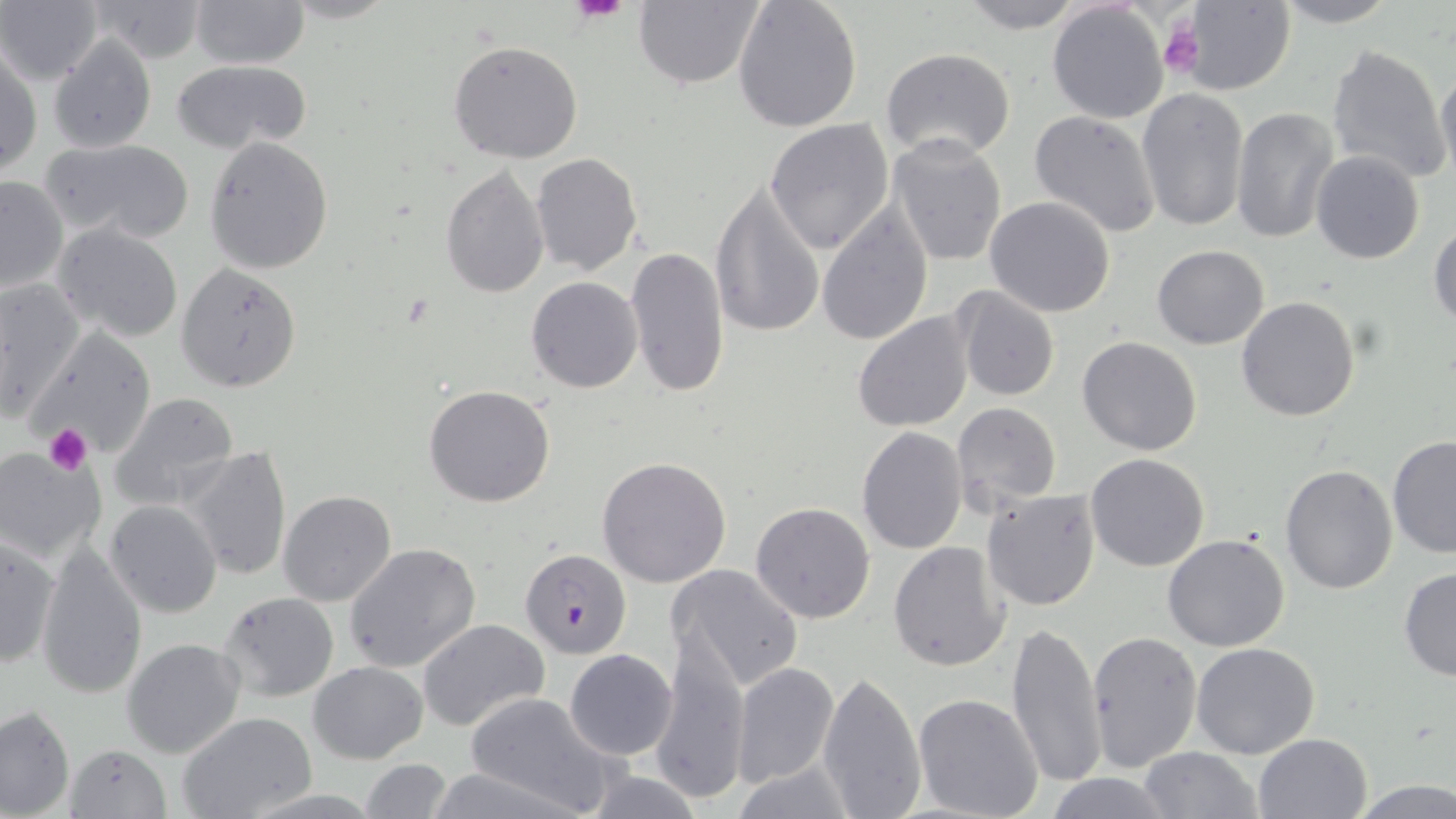
Summary:
  - Coordinate format: approximate bounding boxes as (x1, y1, x2, y2) in pixels
  - Uninfected red blood cell locations: (93, 0, 209, 64), (189, 0, 308, 69), (632, 0, 764, 89), (732, 0, 862, 134), (957, 0, 1086, 33), (1270, 0, 1403, 27), (2, 1, 102, 86), (1181, 1, 1294, 95), (1047, 3, 1170, 125), (48, 33, 156, 152), (448, 40, 583, 164), (1326, 43, 1450, 184), (2, 45, 42, 178), (880, 47, 1016, 161), (172, 58, 311, 154), (1435, 68, 1456, 185), (1136, 87, 1252, 234), (1230, 108, 1340, 245), (1030, 111, 1162, 237), (764, 119, 895, 255), (886, 134, 1008, 269), (42, 138, 194, 243), (205, 138, 332, 274), (1311, 150, 1425, 264), (531, 154, 642, 276), (440, 164, 549, 298), (0, 177, 67, 294), (710, 181, 827, 341), (984, 196, 1116, 318), (815, 202, 935, 348), (1428, 220, 1456, 329), (51, 223, 185, 346), (1152, 244, 1270, 348), (625, 246, 730, 398), (177, 261, 304, 394), (525, 275, 643, 394), (1, 277, 86, 420), (951, 286, 1059, 400), (1236, 297, 1361, 422), (851, 309, 976, 432), (32, 329, 159, 459), (1077, 336, 1204, 456), (424, 384, 555, 507), (109, 393, 240, 511), (953, 402, 1061, 511), (857, 425, 968, 555), (1388, 435, 1456, 560), (184, 445, 293, 582), (0, 448, 106, 567), (1085, 453, 1211, 572), (596, 456, 732, 588), (1281, 463, 1400, 595), (981, 488, 1103, 612), (277, 490, 397, 606), (106, 500, 223, 617), (751, 501, 875, 623), (0, 533, 59, 671), (1162, 533, 1291, 653), (36, 539, 147, 702), (887, 541, 1011, 671), (343, 542, 480, 672), (667, 563, 805, 694), (1398, 566, 1456, 682), (217, 591, 339, 703), (416, 618, 550, 732), (1008, 620, 1104, 791), (651, 630, 752, 806), (1088, 630, 1202, 771), (121, 637, 246, 757), (1190, 642, 1321, 759), (564, 649, 678, 760), (308, 660, 428, 766), (731, 663, 839, 788), (815, 668, 927, 819), (463, 691, 620, 818), (912, 693, 1043, 819), (0, 704, 75, 818), (176, 712, 317, 819), (1252, 731, 1373, 819), (65, 743, 173, 819), (1138, 747, 1263, 819), (357, 759, 453, 819), (728, 759, 856, 818), (571, 764, 709, 819), (1040, 773, 1180, 818), (1347, 779, 1455, 819)
  - Platelet locations: (569, 0, 630, 24), (1157, 19, 1201, 79), (43, 424, 93, 475)
  - Plasmodium falciparum-infected red blood cell locations: (519, 546, 633, 659)
  - Slide-level diagnosis: Plasmodium falciparum
  - Modality: optical microscopy
  - Preparation: thin blood film
  - Stain: May-Grünwald-Giemsa
  - Magnification: 1000x
  - Image size: 1456×819 pixels
  - Field of view: single